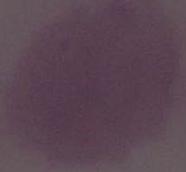

Summary:
  - Identification: erythrocyte
  - Magnification: 1000x
  - Modality: photomicrograph